Assess this cell for malaria.
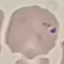

It is uninfected.

Summary:
  - Preparation: thin smear
  - Stain: Giemsa
  - Image type: cell patch, automatically extracted from a larger field of view and resized to 64 × 64 pixels
  - Capture: smartphone through the microscope eyepiece